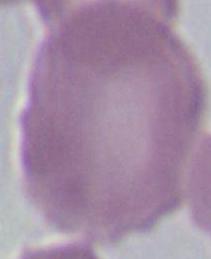

Micrograph. 1000x magnification. A red blood cell is shown.